Give the extent of all Plasmodium falciparum-infected red blood cells.
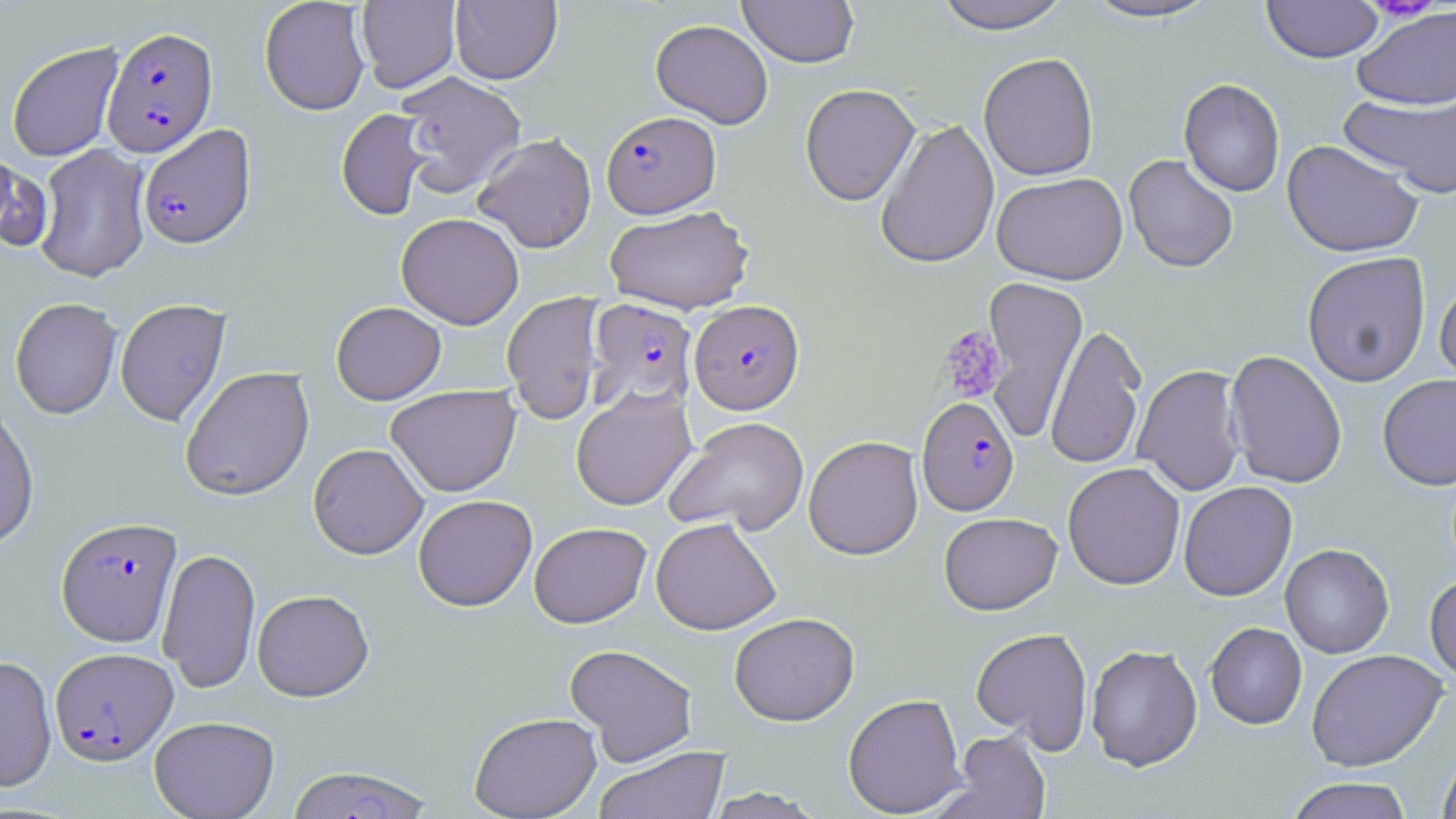

Approximate bounding boxes as (x1,y1)-(x2,y2) corner pairs in pixels.
Plasmodium falciparum-infected red blood cells: (101,26)-(218,157), (601,111)-(721,218), (137,124)-(256,249), (586,298)-(698,410), (689,300)-(804,415), (917,396)-(1019,515), (56,516)-(182,646), (50,646)-(178,764), (285,765)-(435,819).

slide-level diagnosis = Plasmodium falciparum
field of view = one of a larger specimen
magnification = 1000x
platelet locations = approximate bounding boxes as (x1,y1)-(x2,y2) corner pairs in pixels: (938,325)-(1007,403)
modality = light microscopy
uninfected red blood cell locations = approximate bounding boxes as (x1,y1)-(x2,y2) corner pairs in pixels: (259,0)-(371,115), (356,0)-(461,93), (450,0)-(562,84), (738,0)-(858,67), (931,0)-(1074,33), (1079,0)-(1222,23), (1261,1)-(1384,63), (1352,5)-(1456,111), (651,19)-(773,128), (6,41)-(124,162), (978,52)-(1099,181), (394,71)-(526,197), (1179,78)-(1285,197), (800,83)-(920,205), (1339,89)-(1456,199), (336,108)-(434,221), (875,118)-(999,269), (473,133)-(597,253), (1282,139)-(1424,258), (33,144)-(152,283), (1124,154)-(1239,273), (991,172)-(1128,285), (603,205)-(754,315), (396,212)-(524,329), (1302,251)-(1431,387), (1435,274)-(1456,393), (980,276)-(1087,442), (501,291)-(606,424), (10,297)-(122,419), (114,298)-(231,427), (331,301)-(446,404), (1045,323)-(1147,470), (1225,350)-(1348,488), (1133,364)-(1246,496), (179,366)-(314,500), (1377,373)-(1456,490), (386,385)-(521,497), (570,387)-(696,511), (0,405)-(40,551), (664,416)-(809,537), (804,435)-(924,560), (308,443)-(429,559), (1063,462)-(1185,590), (1178,481)-(1297,601), (413,494)-(537,611), (939,512)-(1062,615), (651,517)-(781,635), (529,522)-(651,627), (1280,544)-(1394,658), (157,547)-(261,694), (1425,573)-(1456,686), (252,589)-(374,701), (729,611)-(859,726), (1205,622)-(1307,729), (971,627)-(1093,751), (564,644)-(699,765), (1086,644)-(1203,771), (1307,648)-(1448,771), (0,654)-(57,792), (843,693)-(967,817), (469,712)-(602,818), (149,715)-(280,819), (945,730)-(1051,819), (593,745)-(729,819), (1436,748)-(1456,819), (1284,777)-(1415,819), (703,788)-(828,818)
preparation = thin blood smear
image size = 1456×819 pixels
stain = May-Grünwald-Giemsa